Assess this cell for malaria.
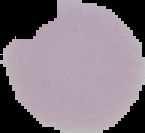

Uninfected.

{
  "image_type": "segmented cell region on a black background",
  "image_size": "145×133 pixels",
  "preparation": "thin blood film"
}